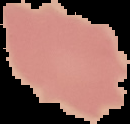
{
  "image_type": "segmented cell region with the area outside set to black",
  "result": "negative for malaria parasites",
  "preparation": "thin blood smear",
  "image_size": "130×124 pixels"
}